Describe the morphology of the erythrocytes.
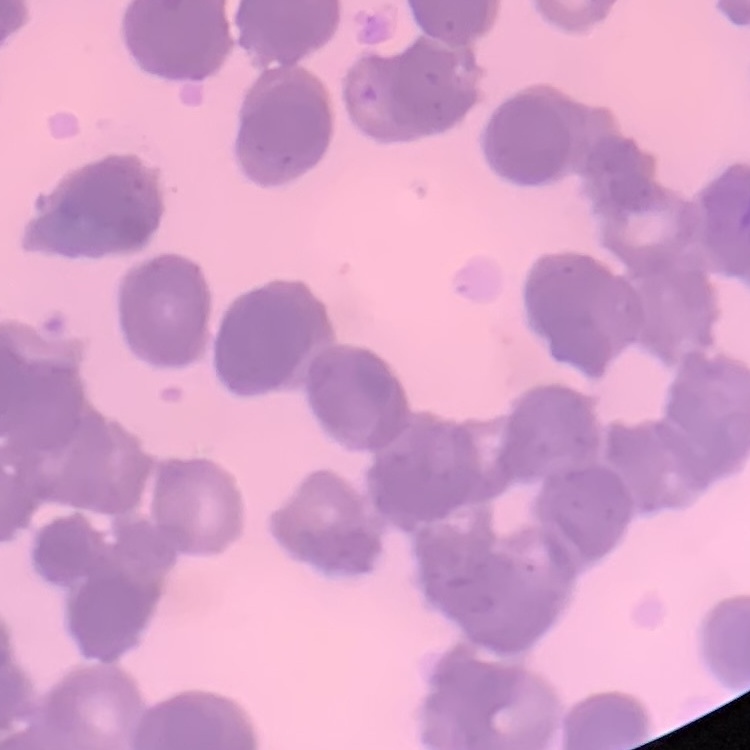

They show rouleaux formation.

One tile cut from a larger photomicrograph. Stained with either Field's or Giemsa. Thin blood smear.